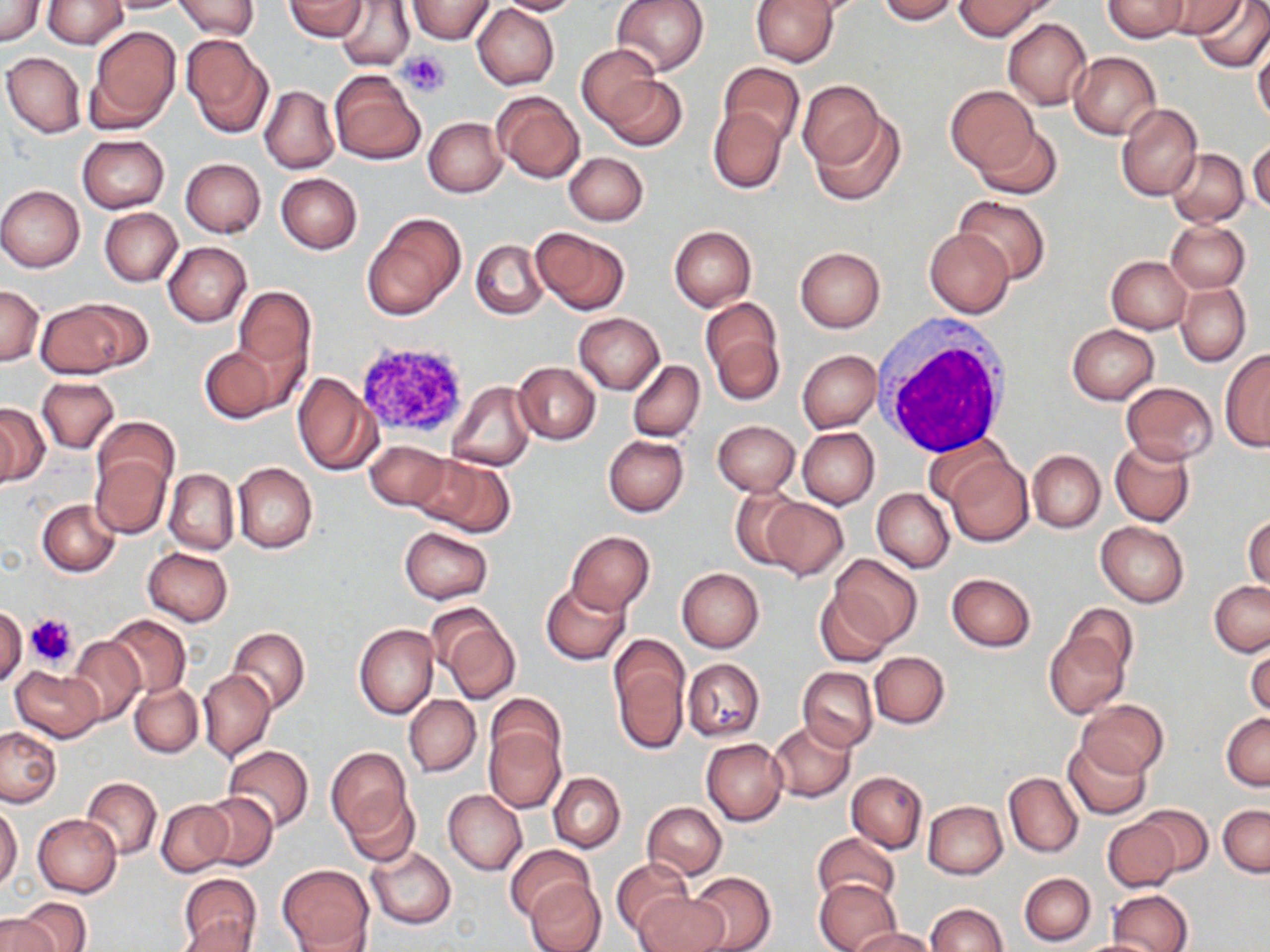

slide_level_diagnosis: no evidence of blood parasites
platelet_locations: 'approximate bounding boxes as (x1,y1)-(x2,y2) corner pairs in pixels: (398,50)-(451,96), (356,339)-(473,437), (26,613)-(76,668)'
stain: May-Grünwald-Giemsa
magnification: 1000x
field_of_view: one of a larger specimen
white_blood_cell_locations: 'approximate bounding boxes as (x1,y1)-(x2,y2) corner pairs in pixels: (877,320)-(1014,456)'
preparation: thin blood film
image_size: 1270×952 pixels
uninfected_red_blood_cell_locations: 'approximate bounding boxes as (x1,y1)-(x2,y2) corner pairs in pixels: (0,0)-(45,46), (41,0)-(129,49), (102,0)-(194,13), (171,0)-(260,38), (284,0)-(368,41), (333,0)-(415,72), (495,0)-(582,16), (612,0)-(709,76), (751,0)-(837,67), (875,0)-(961,23), (955,0)-(1053,41), (1103,0)-(1188,42), (1157,0)-(1243,38), (1192,0)-(1270,73), (406,1)-(495,43), (471,4)-(558,90), (1003,19)-(1091,109), (86,26)-(181,131), (182,35)-(273,137), (1252,40)-(1270,125), (578,44)-(664,129), (1070,51)-(1161,138), (2,52)-(86,137), (716,62)-(804,149), (329,69)-(426,164), (601,75)-(687,151), (798,81)-(884,173), (260,85)-(338,174), (947,85)-(1037,173), (491,90)-(585,183), (1117,104)-(1202,201), (708,105)-(787,195), (807,107)-(904,206), (424,117)-(506,197), (971,123)-(1062,199), (77,135)-(169,213), (1247,139)-(1270,214), (1166,149)-(1249,226), (565,152)-(647,225), (181,158)-(266,237), (276,174)-(363,253), (0,185)-(85,271), (955,195)-(1049,283), (99,208)-(182,287), (362,211)-(466,320), (1166,221)-(1249,292), (669,225)-(757,311), (531,226)-(629,315), (924,229)-(1014,317), (471,240)-(547,320), (164,242)-(251,327), (795,246)-(885,332), (1106,255)-(1193,333), (1175,282)-(1249,366), (0,285)-(43,365), (234,286)-(313,379), (701,297)-(784,403), (33,299)-(140,379), (573,312)-(664,393), (1068,324)-(1158,404), (198,344)-(284,423), (797,350)-(880,433), (1219,350)-(1270,451), (628,360)-(705,443), (514,362)-(600,444), (292,371)-(379,476), (36,377)-(119,453), (447,382)-(536,471), (1121,382)-(1219,466), (0,403)-(48,485), (92,417)-(178,499), (713,420)-(800,496), (797,427)-(878,509), (924,432)-(1013,508), (603,435)-(689,516), (1109,438)-(1195,526), (363,439)-(451,512), (1028,450)-(1105,533), (413,453)-(516,536), (943,454)-(1033,547), (90,455)-(171,537), (233,462)-(317,553), (163,468)-(238,554), (731,488)-(807,570), (872,488)-(954,572), (757,496)-(848,581), (38,498)-(121,576), (1244,513)-(1269,592), (1096,523)-(1189,607), (400,528)-(493,604), (565,531)-(655,615), (142,547)-(232,626), (831,554)-(921,646), (676,567)-(764,652), (946,572)-(1036,652), (541,581)-(630,664), (1209,581)-(1270,657), (814,588)-(896,667), (427,603)-(520,703), (0,606)-(27,688), (104,613)-(190,698), (1043,614)-(1132,719), (354,623)-(439,719), (228,627)-(310,712), (66,636)-(145,724), (609,636)-(690,754), (1246,642)-(1270,721), (870,651)-(950,728), (683,658)-(765,741), (10,665)-(103,741), (797,667)-(877,752), (198,669)-(275,762), (130,682)-(203,757), (486,693)-(564,771), (404,695)-(481,777), (1078,698)-(1167,779), (1223,713)-(1270,791), (769,720)-(855,801), (1,726)-(61,809), (484,727)-(565,813), (701,737)-(787,825), (1063,739)-(1150,819), (221,745)-(315,831), (325,747)-(414,846), (847,771)-(926,853), (1004,772)-(1083,858), (549,773)-(625,852), (81,777)-(162,859), (442,788)-(527,874), (343,790)-(421,867), (198,792)-(278,870), (157,799)-(233,877), (643,801)-(726,879), (923,801)-(1007,878), (0,804)-(22,890), (1134,804)-(1213,876), (1218,804)-(1270,877), (33,814)-(122,897), (1102,817)-(1180,892), (812,832)-(900,908), (505,844)-(595,924), (366,846)-(455,930), (610,858)-(695,939), (277,863)-(374,951), (686,871)-(776,952), (176,873)-(262,950), (1019,873)-(1094,945), (815,878)-(901,952), (524,880)-(604,952), (1107,890)-(1194,952), (636,892)-(728,952), (13,898)-(91,952), (925,903)-(1007,952), (0,912)-(61,952), (176,915)-(256,952), (854,928)-(935,952), (1073,937)-(1168,952)'
modality: light microscopy